Outline each blood parasite and name the species.
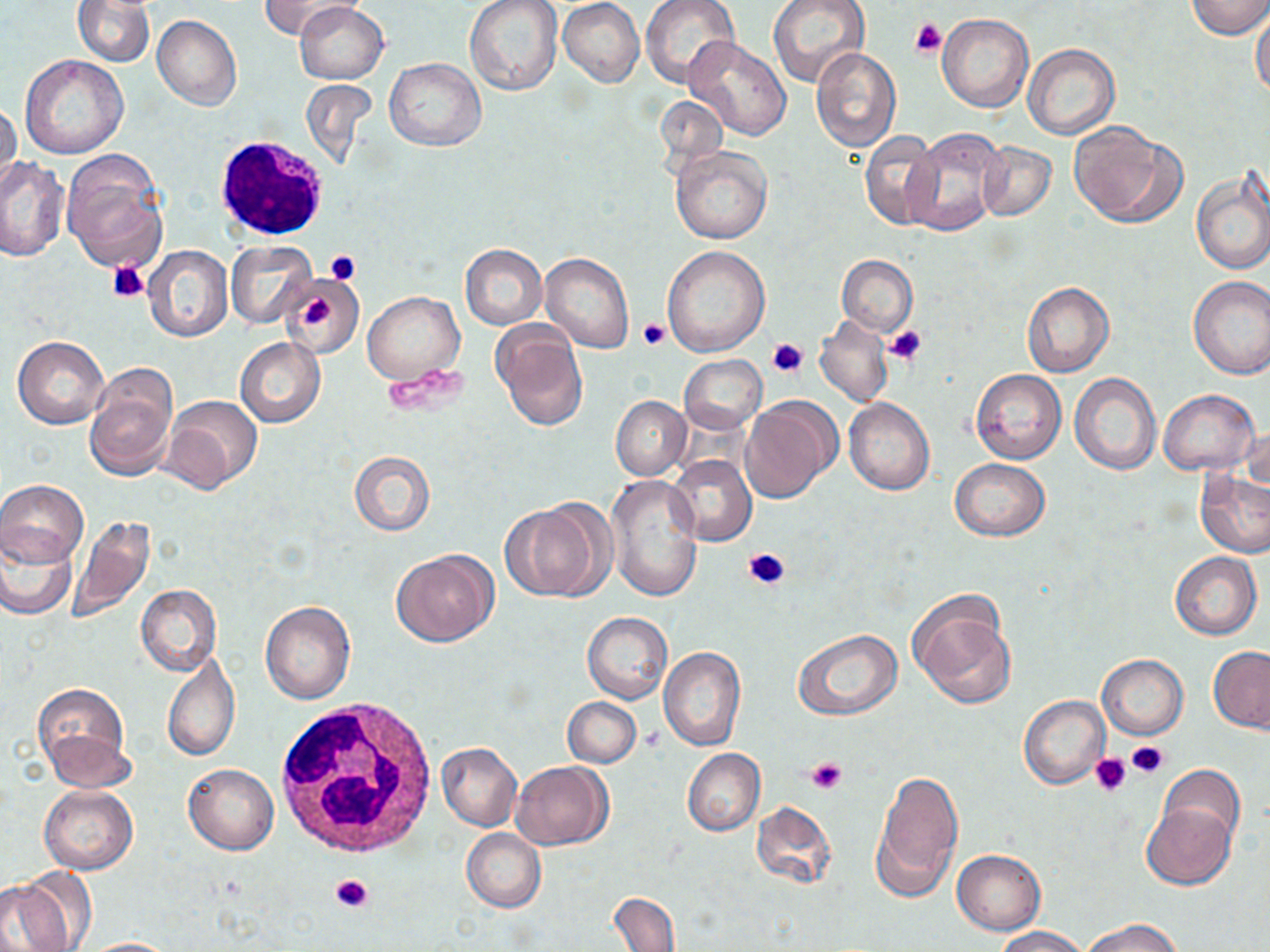
No blood parasites observed.

Approximate bounding boxes as (x1, y1, x2, y2) in pixels. Uninfected red blood cell locations: (73, 0, 155, 66), (258, 0, 358, 39), (559, 0, 643, 87), (640, 0, 741, 87), (767, 0, 870, 88), (1186, 0, 1270, 38), (465, 1, 562, 99), (295, 3, 388, 84), (1251, 9, 1270, 99), (936, 14, 1033, 113), (153, 15, 241, 111), (684, 37, 792, 141), (1023, 44, 1120, 139), (808, 46, 900, 151), (19, 55, 127, 159), (384, 57, 487, 152), (0, 102, 21, 191), (1069, 122, 1183, 228), (860, 129, 944, 229), (904, 129, 1010, 236), (977, 140, 1056, 222), (672, 145, 773, 246), (61, 154, 167, 272), (0, 157, 68, 261), (1192, 170, 1270, 275), (227, 241, 317, 327), (143, 245, 233, 343), (460, 245, 547, 329), (662, 245, 771, 357), (540, 253, 635, 353), (837, 255, 918, 335), (282, 274, 364, 361), (1187, 276, 1270, 379), (1022, 281, 1114, 377), (363, 292, 464, 383), (815, 316, 892, 408), (490, 320, 588, 431), (13, 336, 109, 429), (235, 338, 325, 428), (680, 355, 766, 434), (84, 366, 178, 480), (970, 369, 1066, 465), (1069, 372, 1161, 476), (1159, 389, 1259, 476), (163, 395, 264, 494), (611, 395, 690, 481), (739, 396, 841, 504), (844, 398, 934, 496), (1242, 423, 1269, 502), (349, 450, 435, 537), (667, 454, 756, 547), (949, 458, 1050, 542), (1196, 469, 1270, 558), (607, 474, 702, 603), (0, 480, 88, 568), (501, 500, 606, 600), (65, 516, 156, 623), (0, 528, 76, 619), (392, 549, 497, 646), (1169, 552, 1263, 640), (136, 585, 222, 676), (908, 591, 1017, 709), (261, 600, 356, 705), (582, 611, 672, 704), (792, 628, 902, 722), (1208, 646, 1270, 733), (659, 647, 746, 752), (161, 650, 239, 764), (1097, 653, 1188, 739), (33, 683, 131, 783), (1019, 695, 1109, 789), (562, 697, 640, 768), (437, 743, 522, 831), (683, 748, 765, 836), (512, 761, 613, 849), (183, 763, 278, 855), (1155, 765, 1247, 854), (870, 766, 962, 900), (40, 785, 137, 876), (1141, 800, 1237, 889), (756, 801, 837, 887), (461, 829, 546, 913), (952, 849, 1045, 934), (1, 871, 85, 952), (609, 892, 680, 952), (1080, 916, 1186, 952), (992, 926, 1093, 951), (77, 937, 184, 951). Platelet locations: (911, 18, 947, 58), (326, 250, 360, 283), (108, 261, 149, 303), (303, 297, 334, 327), (638, 318, 669, 350), (887, 326, 928, 363), (768, 338, 808, 376), (385, 366, 468, 416), (742, 547, 789, 588), (1127, 741, 1168, 778), (1089, 753, 1131, 795), (806, 755, 847, 793), (330, 873, 376, 914). White blood cell locations: (214, 135, 331, 242), (274, 700, 439, 857). Slide-level diagnosis: no evidence of blood parasites. May-Grünwald-Giemsa stain. Thin blood smear. Single field of view. Captured at 1000x magnification. Image is 1270×952 pixels. Optical microscopy.